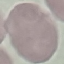 Result: no malaria parasites detected. Acquired by smartphone through the microscope eyepiece. Giemsa stain. Cell patch, automatically extracted from a larger field of view and resized to 64 × 64 pixels. Thin smear of blood.